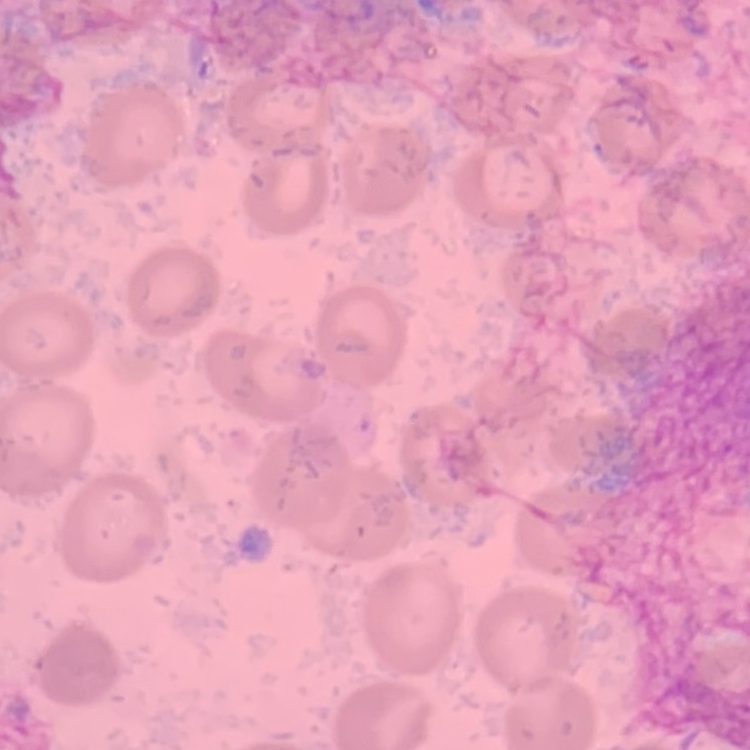
Summary:
  - Red blood cell morphology: no rouleaux formation
  - Preparation: thin blood film
  - Stain: Field's or Giemsa
  - Image type: square crop of a larger photomicrograph